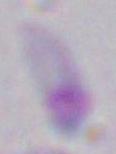

Photomicrograph. Toxoplasma gondii is shown. Captured at 1000x magnification.